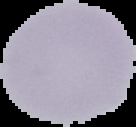 Result: negative for malaria parasites. From a thin blood film. Image is 136×127 pixels. Cell region segmented out of the field of view; the surrounding area is masked to black.